Classify this cell by malaria status.
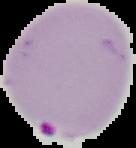

It is parasitized.

image size = 136×148 pixels
preparation = thin blood film
image type = segmented cell region on a black background